Describe the morphology of the erythrocytes.
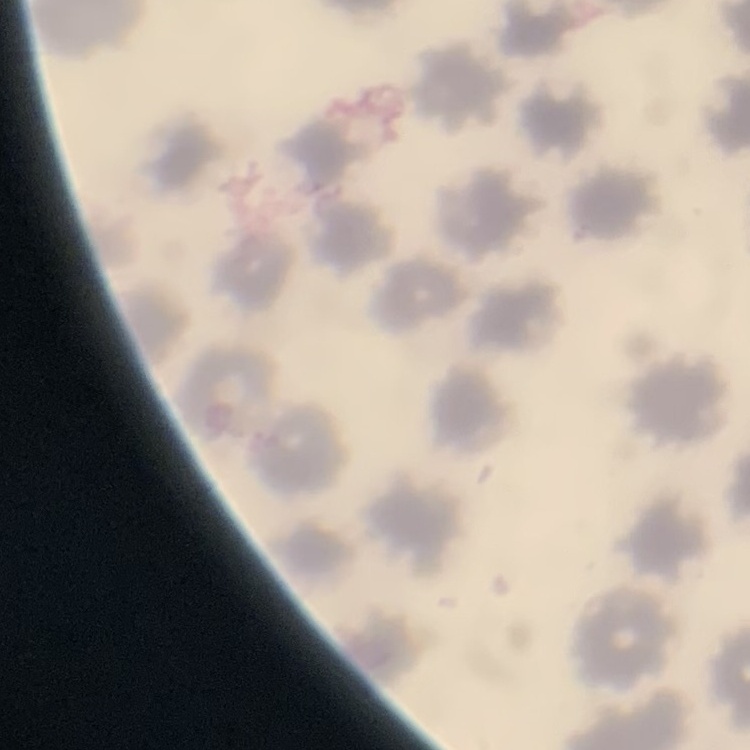
They show no rouleaux formation.

Thin peripheral smear. Stained with either Field's or Giemsa. Square crop of a larger photomicrograph.